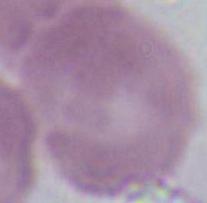
A red blood cell is seen. Photomicrograph. 1000x magnification.